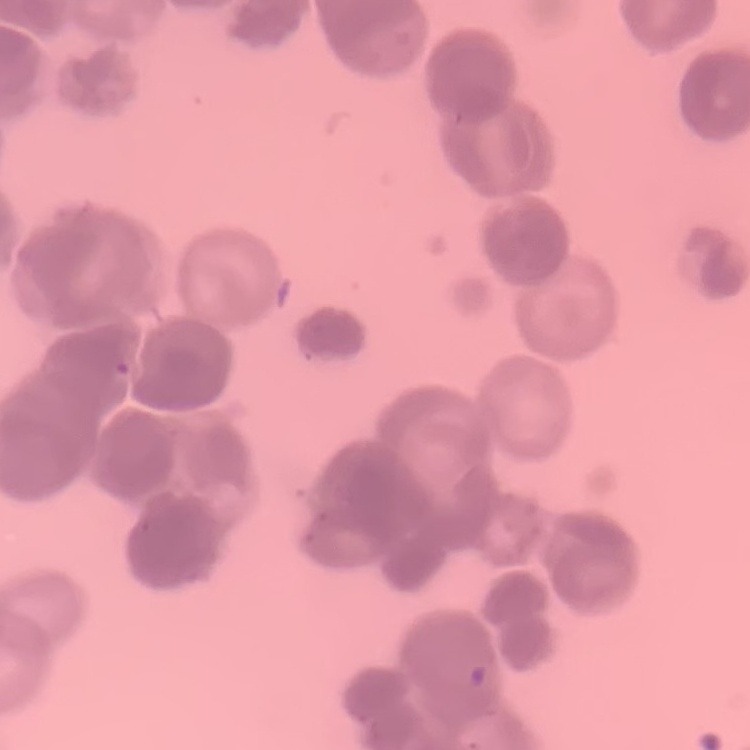

The erythrocytes show rouleaux formation. Square crop of a larger photomicrograph. Thin blood smear. Stained with either Field's or Giemsa.